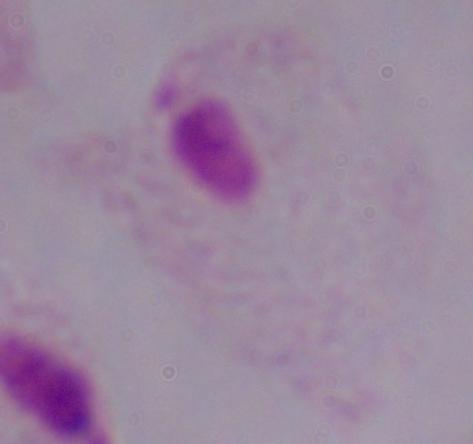
magnification = 1000x
modality = photomicrograph
identification = trichomonad